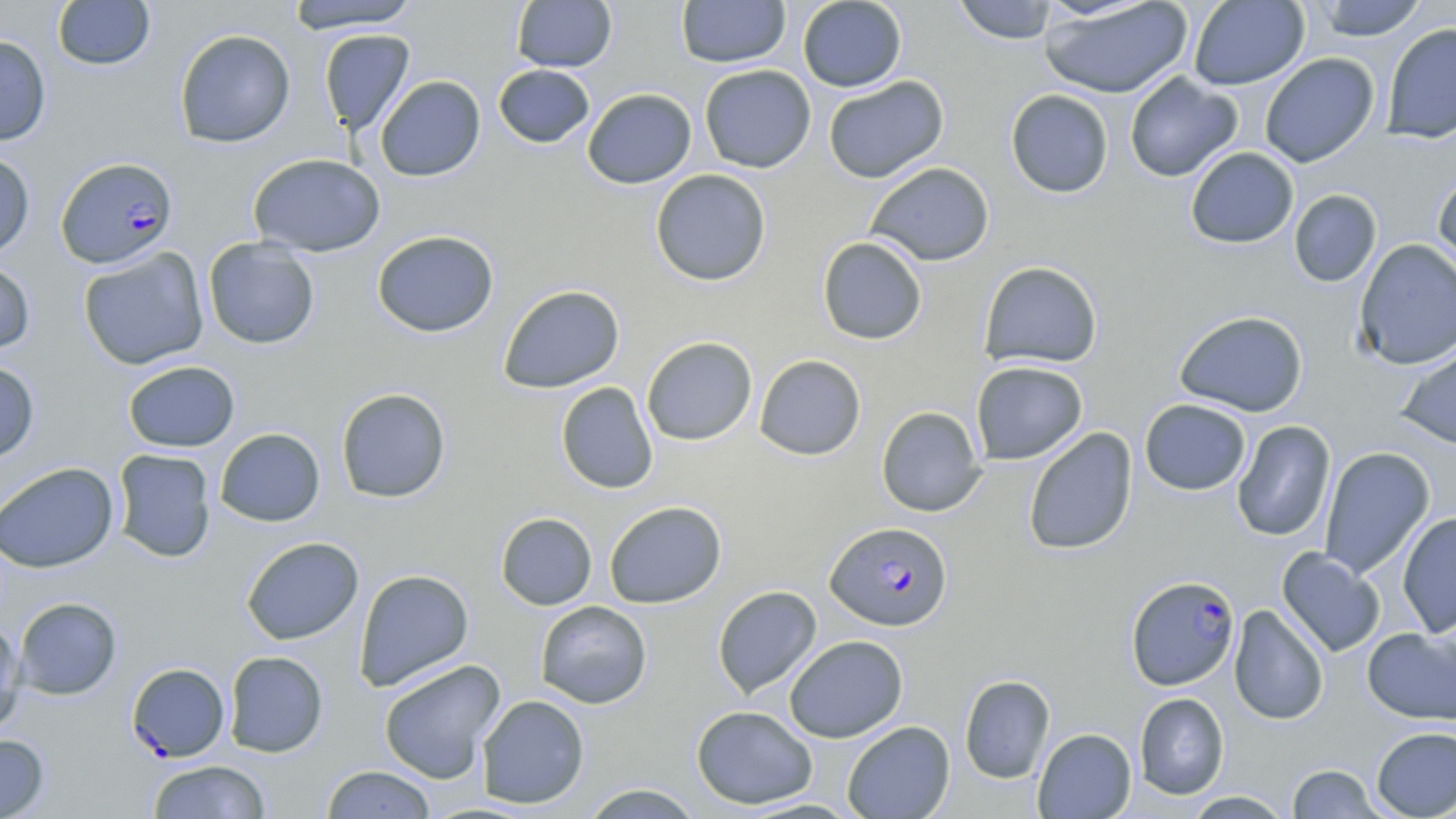
Approximate bounding boxes as [x1, y1, x2, y2] in pixels. Plasmodium falciparum-infected red blood cell locations: [58, 156, 179, 269], [826, 521, 953, 631], [1126, 575, 1241, 690], [126, 668, 230, 767]. Uninfected red blood cell locations: [52, 0, 155, 70], [511, 0, 618, 73], [676, 0, 791, 68], [797, 0, 907, 92], [951, 0, 1060, 44], [1038, 0, 1193, 99], [1312, 0, 1428, 41], [285, 1, 421, 33], [1189, 1, 1310, 90], [1380, 21, 1456, 145], [173, 28, 296, 148], [318, 29, 416, 136], [0, 35, 51, 146], [1259, 53, 1380, 168], [493, 64, 595, 148], [699, 64, 816, 173], [1124, 72, 1243, 182], [375, 75, 486, 181], [823, 75, 949, 184], [582, 87, 697, 189], [1004, 89, 1114, 198], [1185, 147, 1299, 249], [0, 152, 35, 259], [248, 153, 386, 256], [864, 161, 995, 266], [650, 169, 772, 286], [1432, 170, 1456, 287], [1289, 189, 1382, 288], [372, 229, 499, 338], [817, 236, 928, 345], [203, 237, 320, 349], [1354, 238, 1456, 369], [77, 246, 209, 370], [0, 259, 36, 355], [979, 261, 1103, 369], [498, 284, 625, 394], [1173, 309, 1309, 418], [641, 336, 758, 446], [1396, 339, 1456, 451], [754, 354, 866, 460], [0, 360, 40, 465], [122, 360, 240, 452], [971, 360, 1088, 465], [556, 382, 658, 494], [335, 387, 451, 503], [1139, 399, 1252, 496], [876, 406, 986, 517], [1231, 420, 1336, 542], [214, 427, 326, 527], [1023, 427, 1138, 556], [1318, 446, 1435, 580], [112, 449, 217, 562], [0, 461, 119, 573], [604, 500, 727, 608], [1397, 511, 1456, 638], [495, 512, 597, 610], [241, 536, 364, 645], [1276, 547, 1385, 657], [354, 569, 474, 691], [712, 585, 822, 700], [13, 597, 121, 699], [535, 601, 652, 709], [1228, 604, 1330, 725], [0, 619, 26, 737], [1362, 628, 1456, 725], [784, 635, 908, 743], [223, 651, 329, 757], [378, 659, 506, 784], [959, 674, 1055, 783], [1134, 692, 1229, 800], [477, 694, 590, 809], [691, 705, 818, 809], [842, 721, 955, 819], [1371, 725, 1456, 818], [1032, 728, 1137, 818], [0, 734, 49, 819], [147, 759, 270, 818], [1287, 763, 1385, 818], [321, 765, 437, 818], [578, 783, 704, 818], [1182, 791, 1294, 818]. Slide-level diagnosis: Plasmodium falciparum. Thin blood film. Captured at 1000x magnification. Optical microscopy. May-Grünwald-Giemsa-stained preparation. Image is 1456×819 pixels. Single field of view.